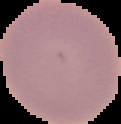
image size = 121×124 pixels
preparation = thin blood film
image type = segmented cell region on a black background
malaria status = uninfected